Identify the parasite.
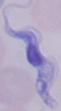

This is a trypanosome.

Photomicrograph. 1000x magnification.